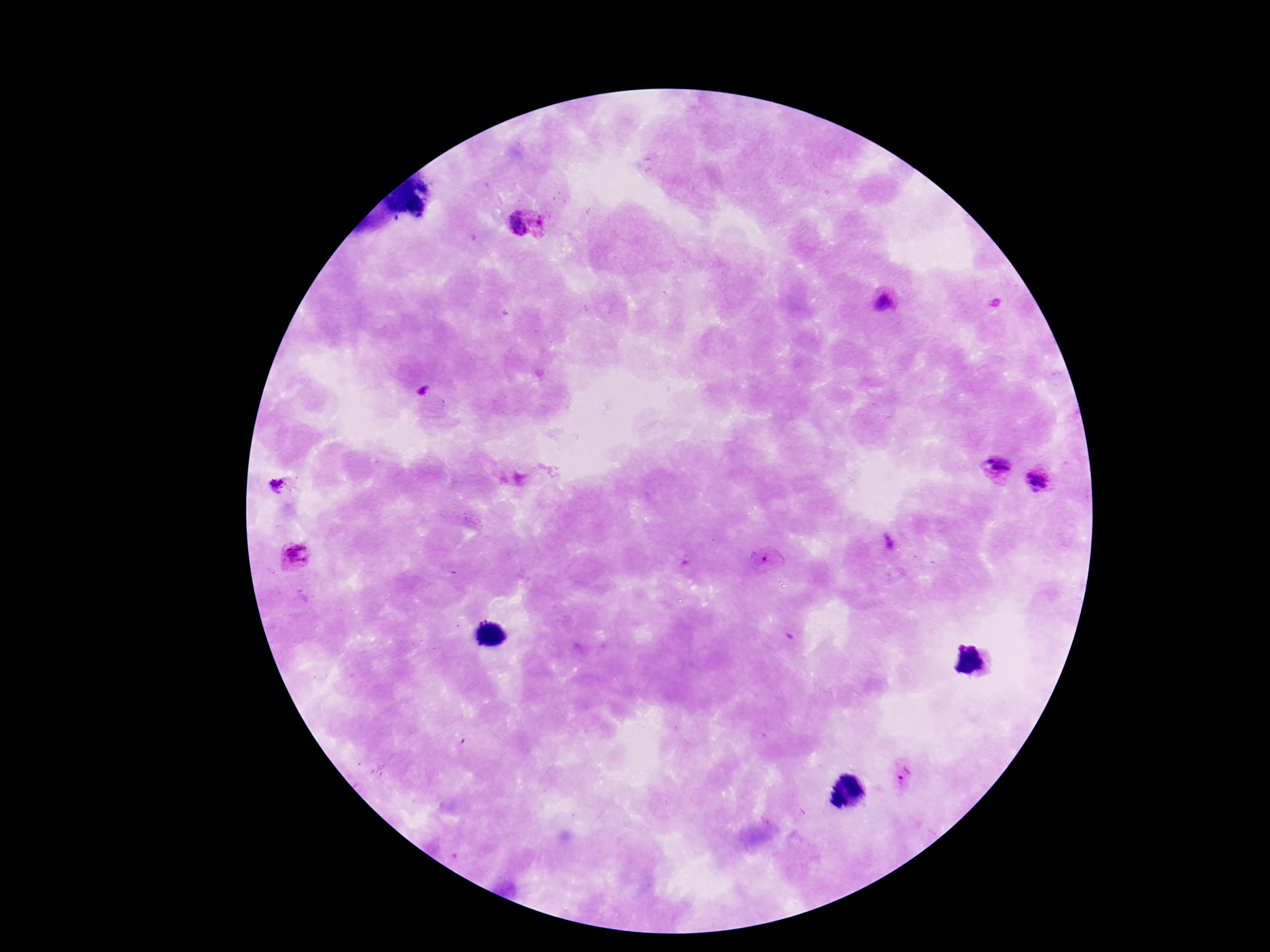
Approximate centers as [x, y] in pixels. Plasmodium parasite locations: [516, 224], [883, 302], [997, 468], [1040, 478], [281, 486], [889, 542], [293, 555], [768, 561], [904, 775]. Patient malaria status: infected. 100x magnification. Giemsa-stained preparation. Thick blood film. Smartphone photograph taken through the microscope eyepiece. Image is 1270×952 pixels. One field from this slide.